Name the parasite shown.
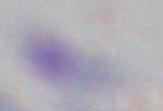
Toxoplasma gondii.

Summary:
  - Modality: photomicrograph
  - Magnification: 1000x